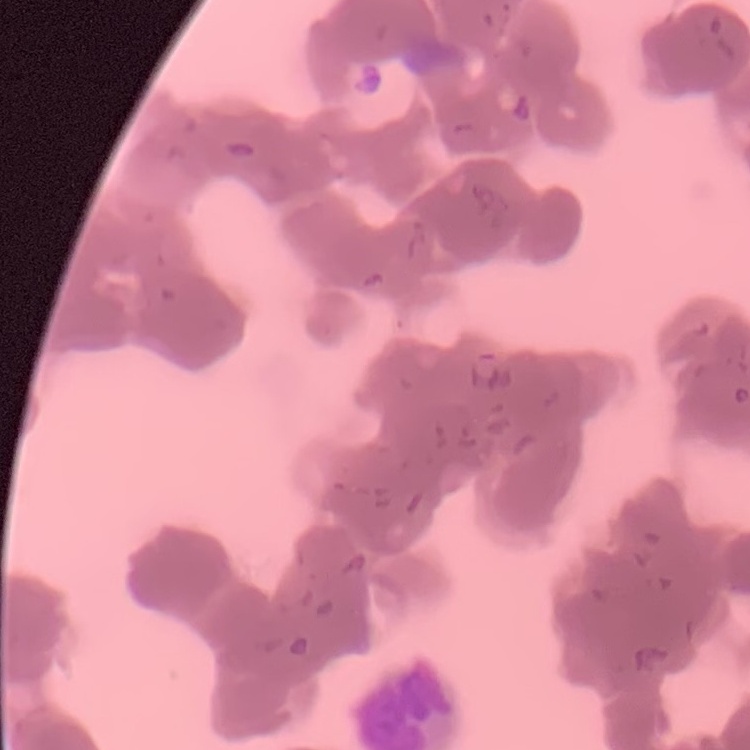

Summary:
  - Erythrocyte morphology: rouleaux formation
  - Image type: square crop of a larger photomicrograph
  - Preparation: thin blood smear
  - Stain: Field's or Giemsa